Identify the parasite.
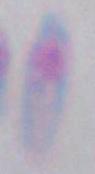
This is Toxoplasma gondii.

Micrograph. 1000x magnification.